Describe the morphology of the erythrocytes.
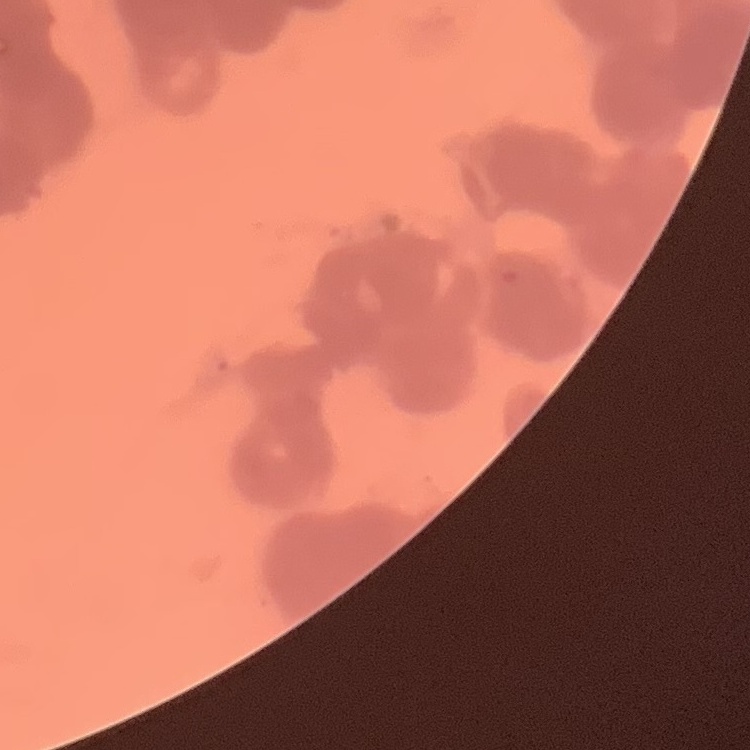
Rouleaux formation.

stain = Field's or Giemsa
preparation = thin blood smear
image type = square crop of a larger photomicrograph